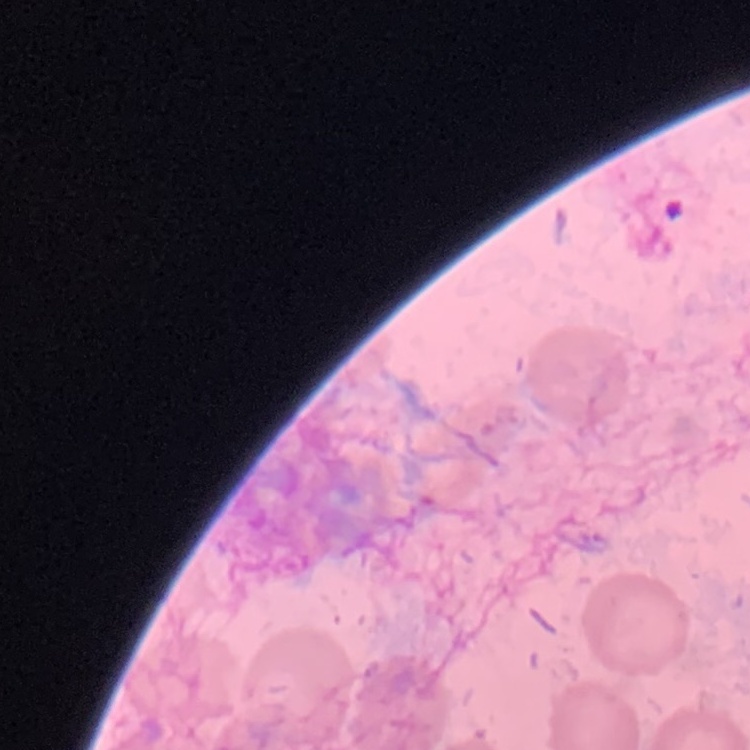
Summary:
  - Red blood cell morphology: no rouleaux formation
  - Preparation: thin blood film
  - Stain: Field's or Giemsa
  - Image type: one tile cut from a larger photomicrograph